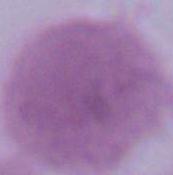

Summary:
  - Modality: photomicrograph
  - Identification: erythrocyte
  - Magnification: 1000x